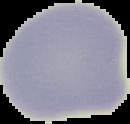
Summary:
  - Preparation: thin blood smear
  - Image size: 130×124 pixels
  - Result: no Plasmodium parasites detected
  - Image type: segmented cell region with the area outside set to black